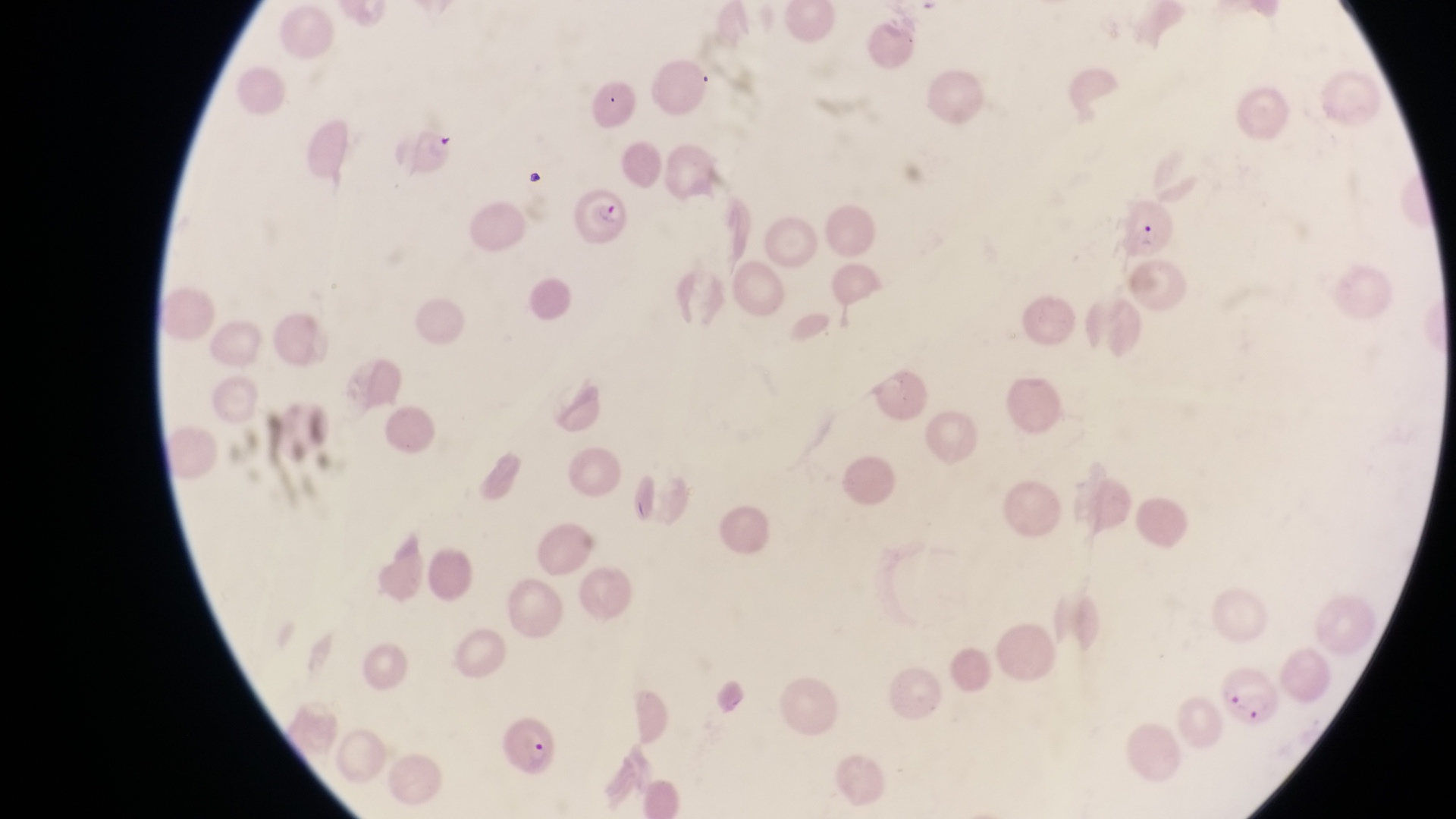

Approximate bounding boxes as {left, top, right, bottom} in pixels.
Summary:
  - Parasitised red blood cell locations: {566, 180, 632, 241}, {492, 717, 556, 780}
  - Preparation: thin blood film
  - Magnification: 1000x
  - Image size: 1456×819 pixels
  - Field of view: single
  - Capture: smartphone photograph through the eyepiece of an Olympus CX-23 microscope
  - Country: Uganda